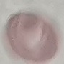
malaria status = uninfected
preparation = thin blood film
stain = Giemsa
image type = cell patch, automatically extracted from a larger field of view and resized to 64 × 64 pixels
capture = smartphone through the microscope eyepiece